Classify this cell by malaria status.
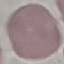
Uninfected.

Acquired by smartphone through the microscope eyepiece. Thin smear of blood. Giemsa stain. Cell patch, automatically extracted from a larger field of view and resized to 64 × 64 pixels.